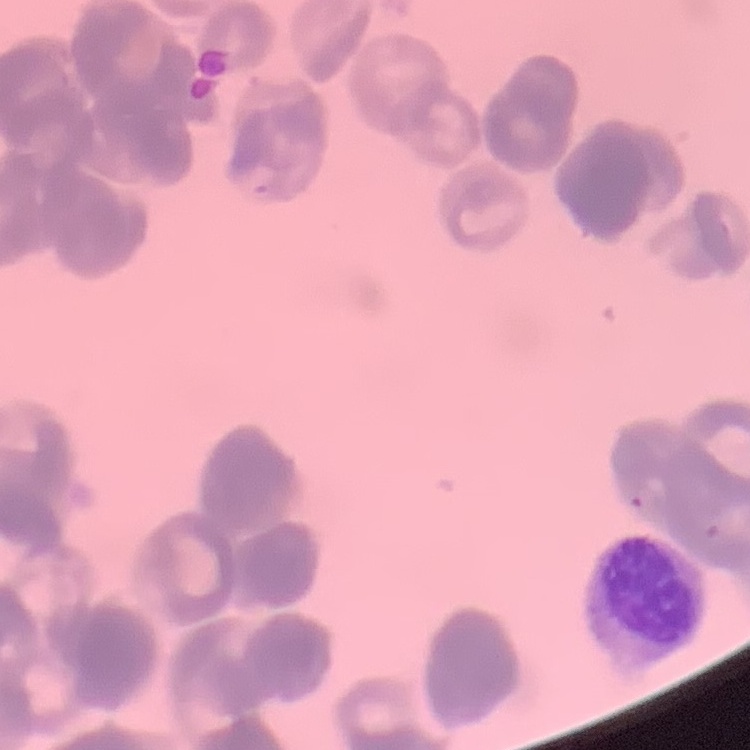

red blood cell morphology = rouleaux formation
image type = square crop of a larger photomicrograph
preparation = thin blood film
stain = Field's or Giemsa